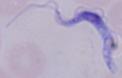

identification = trypanosome
modality = micrograph
magnification = 1000x